Identify the preparation type.
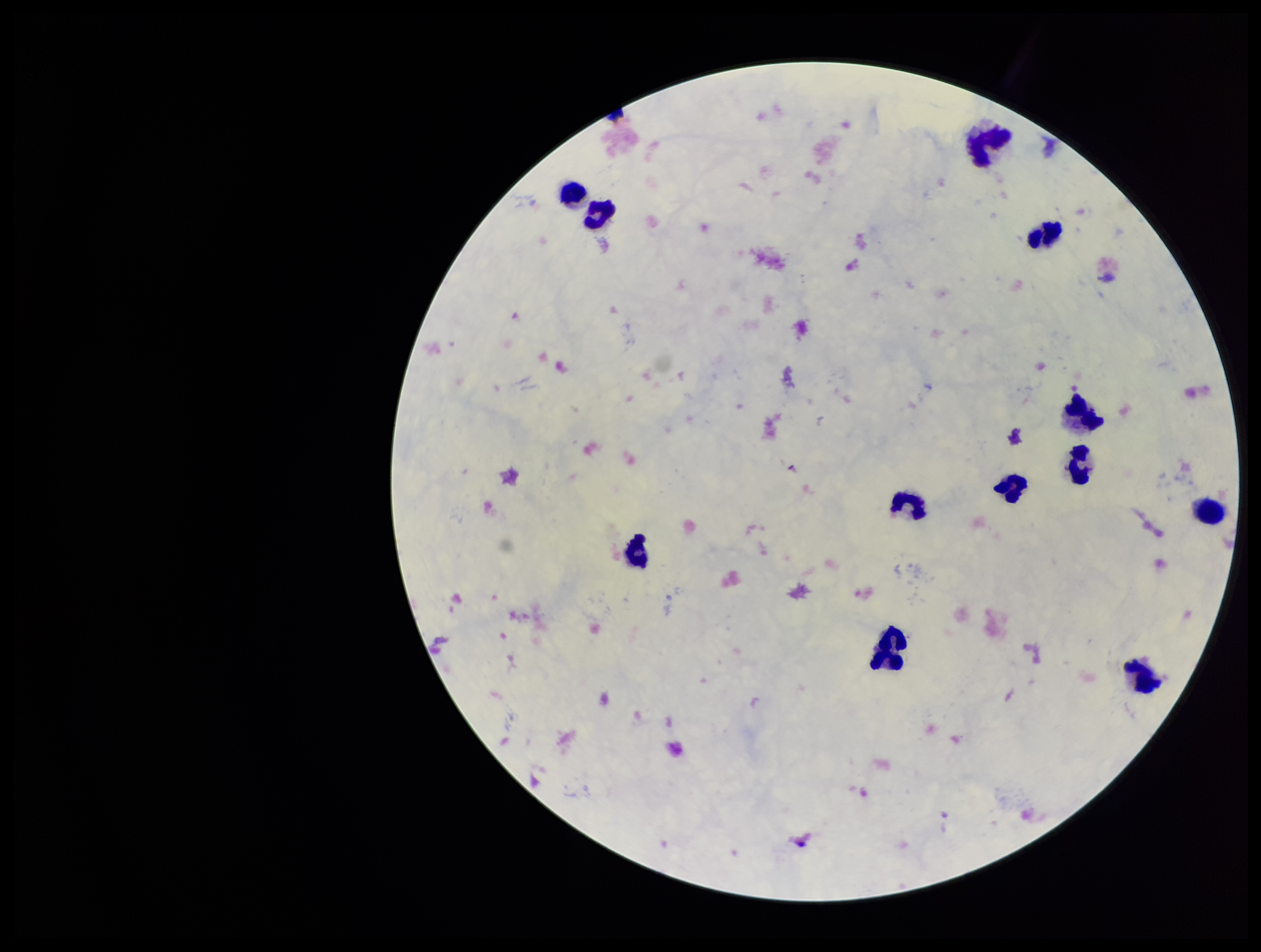

Thick.

stain = Giemsa
image size = 1261×952 pixels
field of view = single
patient malaria status = negative
capture = smartphone photograph through the microscope eyepiece
parasite count = 0
Plasmodium parasites = none identified
leukocyte count = 12